Classify this cell by malaria status.
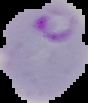

Parasitized.

image_size: 88×103 pixels
preparation: thin blood film
image_type: segmented cell region with the area outside set to black